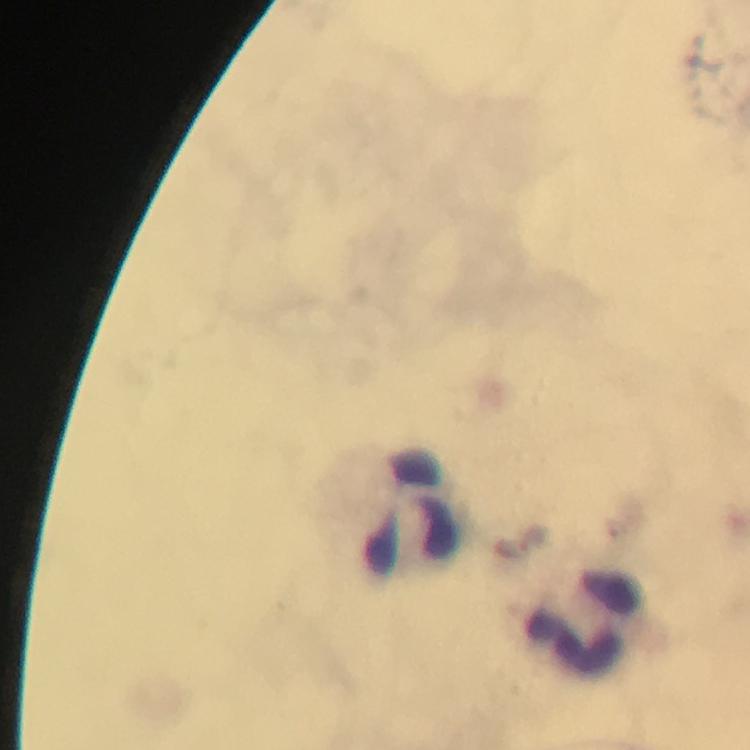

Approximate centers as [x, y] in pixels. Malaria parasite locations: [617, 528], [533, 539]. Leukocyte locations: [413, 510], [584, 623]. 100x magnification. From a diagnostic examination for malaria. Immersion oil applied. Image is 750×750 pixels. Cropped region of a single field of view. Photographed through the microscope with a smartphone camera. Giemsa-stained preparation. Thick blood smear.